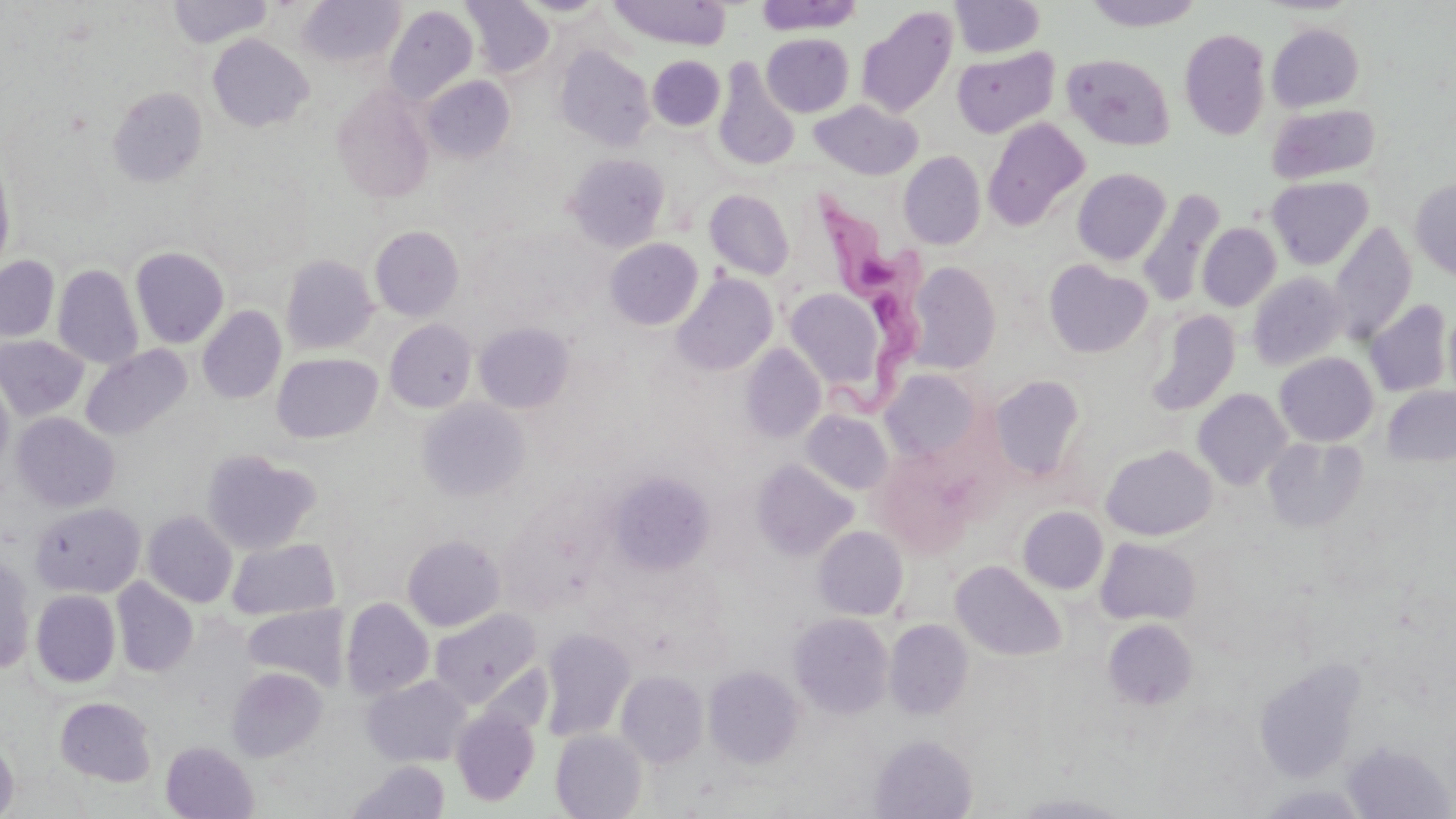
slide_level_diagnosis: Trypanosoma brucei
magnification: 1000x
preparation: thin blood smear
stain: May-Grünwald-Giemsa
modality: light microscopy
image_size: 1456×819 pixels
trypanosoma_brucei_locations: 'approximate bounding boxes as (x1, y1, x2, y2) in pixels: (796, 188, 928, 415)'
field_of_view: one of a larger specimen
uninfected_red_blood_cell_locations: 'approximate bounding boxes as (x1, y1, x2, y2) in pixels: (167, 0, 273, 48), (297, 0, 404, 69), (462, 0, 554, 77), (610, 0, 730, 49), (755, 0, 863, 34), (949, 0, 1045, 58), (1083, 0, 1205, 31), (516, 1, 610, 18), (385, 4, 478, 103), (856, 7, 958, 117), (1267, 22, 1365, 111), (1179, 28, 1271, 140), (762, 33, 854, 117), (207, 34, 314, 132), (555, 46, 655, 151), (951, 46, 1060, 139), (1062, 53, 1174, 150), (648, 56, 725, 131), (713, 59, 801, 172), (421, 75, 516, 162), (331, 85, 435, 204), (107, 87, 207, 188), (810, 100, 923, 180), (1267, 103, 1380, 184), (983, 117, 1090, 230), (0, 151, 15, 278), (899, 151, 986, 249), (565, 154, 669, 252), (1072, 168, 1171, 265), (1266, 175, 1373, 269), (1410, 178, 1456, 282), (1138, 188, 1226, 305), (704, 189, 794, 280), (1328, 222, 1417, 345), (1197, 223, 1281, 311), (370, 226, 464, 321), (605, 239, 703, 330), (130, 247, 229, 348), (0, 255, 60, 342), (281, 255, 378, 354), (1043, 260, 1152, 358), (908, 261, 1001, 373), (53, 265, 143, 369), (672, 272, 777, 376), (1247, 272, 1348, 371), (785, 289, 891, 393), (1365, 299, 1453, 397), (1443, 304, 1456, 406), (197, 306, 287, 404), (1144, 308, 1241, 415), (384, 320, 477, 413), (475, 322, 574, 413), (0, 335, 89, 421), (740, 344, 826, 443), (80, 345, 192, 441), (1274, 352, 1378, 446), (272, 353, 383, 443), (879, 368, 985, 463), (0, 371, 14, 480), (988, 375, 1087, 482), (1382, 386, 1456, 466), (1193, 388, 1292, 490), (417, 398, 529, 501), (801, 410, 893, 495), (11, 412, 120, 512), (1263, 437, 1368, 533), (1101, 445, 1217, 540), (201, 449, 321, 555), (870, 452, 977, 558), (752, 459, 857, 560), (609, 473, 715, 573), (30, 503, 146, 598), (1018, 506, 1108, 595), (142, 510, 237, 607), (813, 525, 908, 620), (402, 535, 505, 631), (1095, 537, 1201, 625), (227, 538, 340, 620), (0, 554, 36, 675), (950, 560, 1066, 661), (112, 578, 198, 677), (31, 590, 121, 687), (341, 598, 434, 700), (242, 604, 349, 690), (430, 608, 541, 707), (789, 612, 894, 718), (883, 619, 973, 719), (1103, 619, 1198, 710), (540, 627, 635, 742), (1254, 658, 1362, 782), (704, 665, 804, 768), (227, 667, 328, 762), (617, 670, 708, 768), (363, 675, 472, 767), (55, 697, 157, 786), (451, 707, 540, 806), (550, 729, 647, 819), (870, 734, 977, 818), (0, 736, 19, 819), (161, 741, 258, 818), (1343, 741, 1454, 819), (348, 760, 450, 818), (1009, 793, 1134, 818)'